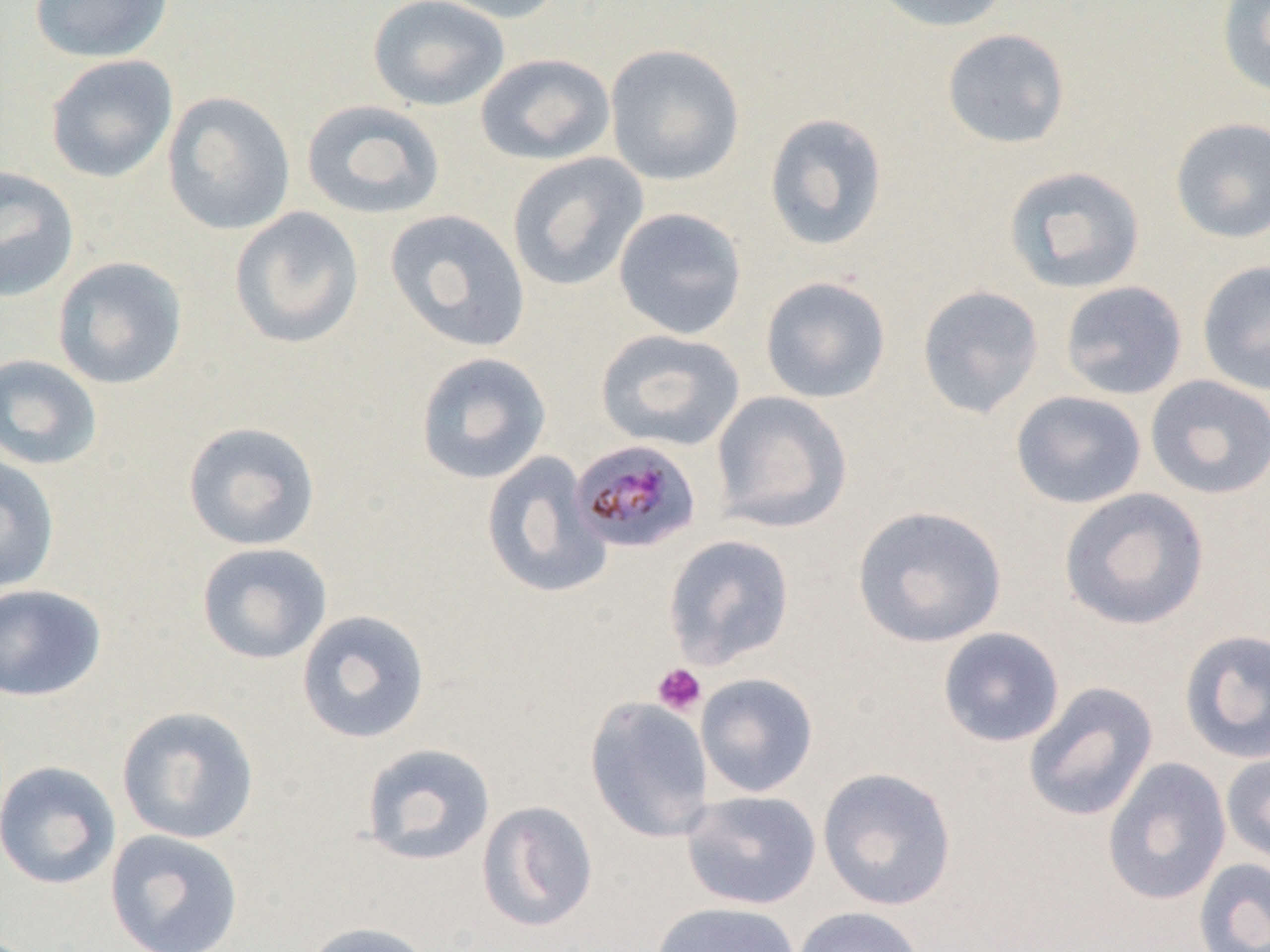 Approximate bounding boxes as (x1,y1)-(x2,y2) corner pairs in pixels. Plasmodium malariae-infected red blood cell locations: (570,440)-(702,554). Platelet locations: (652,663)-(707,716). Uninfected red blood cell locations: (27,0)-(174,63), (367,0)-(510,112), (426,0)-(566,24), (866,0)-(1013,33), (1217,1)-(1270,98), (941,28)-(1071,149), (604,43)-(745,186), (475,53)-(616,166), (45,54)-(178,184), (161,90)-(296,235), (301,99)-(446,220), (763,112)-(888,251), (1168,116)-(1270,244), (507,152)-(649,292), (0,165)-(80,302), (1002,165)-(1147,294), (228,206)-(365,349), (613,207)-(747,340), (383,209)-(531,353), (51,256)-(188,390), (1197,260)-(1270,396), (759,275)-(892,404), (1059,280)-(1188,400), (916,284)-(1044,419), (595,329)-(745,451), (414,351)-(552,484), (0,353)-(103,471), (1144,375)-(1270,499), (710,390)-(853,533), (1010,390)-(1147,509), (182,421)-(321,551), (481,451)-(612,600), (0,453)-(60,593), (1058,488)-(1210,631), (852,504)-(1007,648), (663,534)-(795,669), (195,542)-(333,665), (0,584)-(107,702), (296,609)-(431,744), (937,627)-(1065,748), (1178,629)-(1270,764), (695,673)-(819,798), (1023,681)-(1158,823), (585,696)-(715,842), (115,705)-(260,844), (360,743)-(496,867), (1220,749)-(1270,866), (1102,757)-(1232,906), (0,760)-(121,890), (817,766)-(957,911), (681,790)-(821,910), (476,800)-(599,932), (104,829)-(245,951), (1193,857)-(1270,952), (650,901)-(801,952), (792,906)-(925,952), (300,921)-(435,952). Slide-level diagnosis: Plasmodium malariae. Light microscopy. Captured at 1000x magnification. Thin blood film. Single field of view. Image is 1270×952 pixels.